Classify this cell by malaria status.
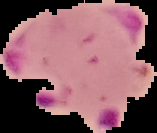
Parasitized.

Summary:
  - Preparation: thin blood film
  - Image size: 157×133 pixels
  - Image type: segmented cell region on a black background